Assess the morphology of the red blood cells.
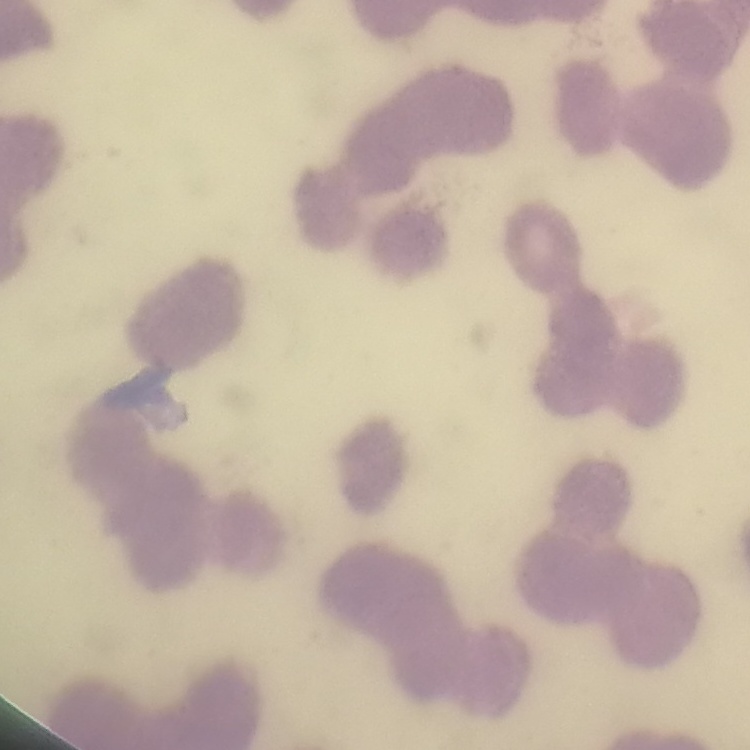

Rouleaux formation.

stain = Field's or Giemsa
image type = one tile cut from a larger photomicrograph
preparation = thin blood smear